Report the malaria status of this cell.
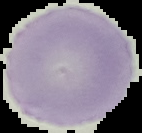

It is uninfected.

Summary:
  - Preparation: thin blood film
  - Image type: segmented cell region with the area outside set to black
  - Image size: 142×133 pixels